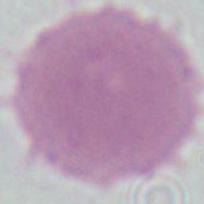
Photomicrograph. 1000x magnification. A red blood cell is shown.